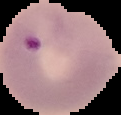

Malaria status: parasitized. Cell region segmented out of the field of view; the surrounding area is masked to black. From a thin blood film. Image is 121×115 pixels.